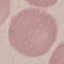

result = no malaria parasites seen
preparation = thin blood smear
stain = Giemsa
capture = smartphone camera at the microscope eyepiece
image type = cell patch, automatically extracted from a larger field of view and resized to 64 × 64 pixels